Classify this cell by malaria status.
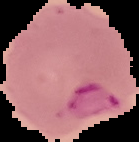

Parasitized.

{
  "image_size": "139×142 pixels",
  "preparation": "thin blood film",
  "image_type": "segmented cell region with the area outside set to black"
}